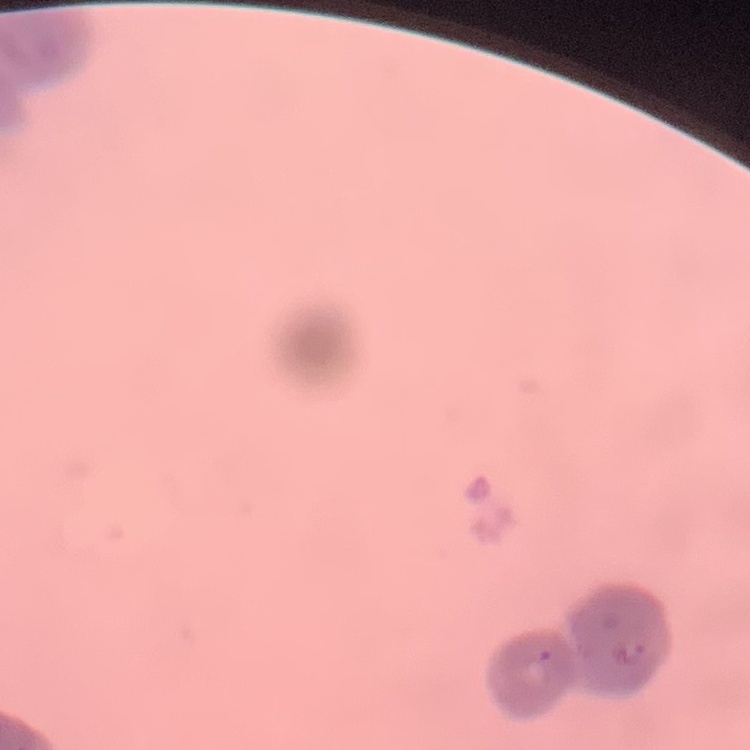

erythrocyte morphology = rouleaux formation
preparation = thin peripheral smear
stain = Field's or Giemsa
image type = one tile cut from a larger photomicrograph